Report the malaria status of this cell.
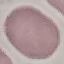

It is uninfected.

Summary:
  - Image type: cell patch, automatically extracted from a larger field of view and resized to 64 × 64 pixels
  - Stain: Giemsa
  - Capture: smartphone camera at the microscope eyepiece
  - Preparation: thin smear